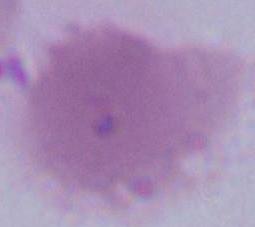

identification = red blood cell
modality = photomicrograph
magnification = 1000x